Classify this cell by malaria status.
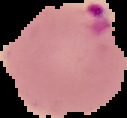
It is parasitized.

preparation = thin blood film
image type = segmented cell region with the area outside set to black
image size = 127×118 pixels